State which cell type is depicted.
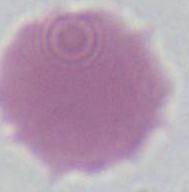
This is an erythrocyte.

Photomicrograph. 1000x magnification.